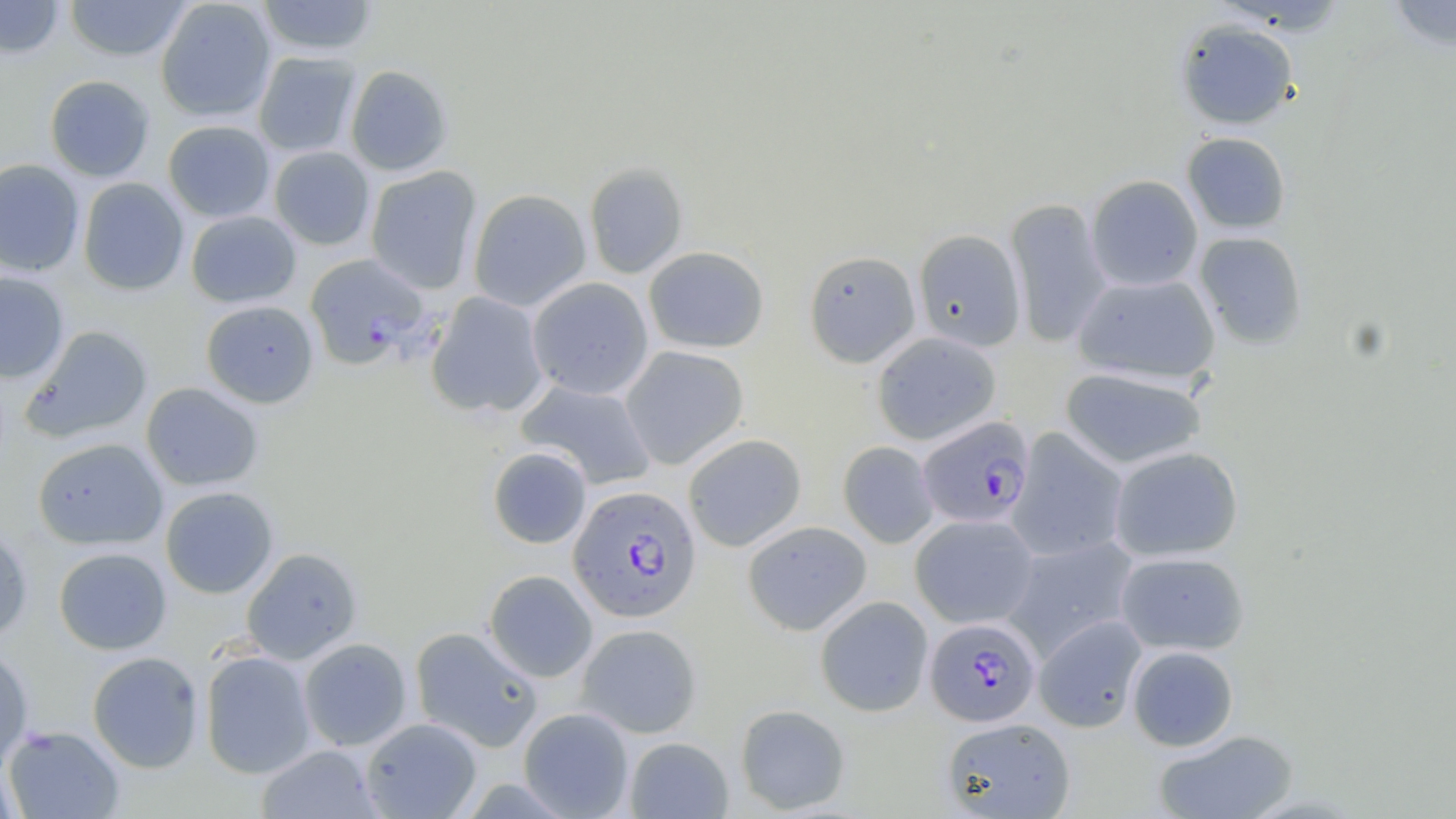
Approximate bounding boxes as named x1/y1/x2/y2 corners in pixels. Uninfected red blood cell locations: (x1=0, y1=0, x2=66, y2=59), (x1=63, y1=0, x2=193, y2=61), (x1=155, y1=0, x2=276, y2=122), (x1=255, y1=0, x2=380, y2=57), (x1=1383, y1=1, x2=1456, y2=52), (x1=1176, y1=19, x2=1299, y2=130), (x1=253, y1=52, x2=361, y2=158), (x1=345, y1=64, x2=453, y2=176), (x1=44, y1=75, x2=156, y2=182), (x1=163, y1=120, x2=275, y2=223), (x1=1181, y1=132, x2=1292, y2=234), (x1=269, y1=146, x2=375, y2=250), (x1=0, y1=158, x2=85, y2=277), (x1=584, y1=163, x2=688, y2=278), (x1=365, y1=166, x2=482, y2=294), (x1=1086, y1=174, x2=1203, y2=292), (x1=77, y1=177, x2=189, y2=295), (x1=468, y1=188, x2=592, y2=312), (x1=1004, y1=197, x2=1112, y2=349), (x1=185, y1=210, x2=301, y2=308), (x1=913, y1=228, x2=1026, y2=352), (x1=1193, y1=231, x2=1308, y2=349), (x1=643, y1=246, x2=769, y2=353), (x1=803, y1=249, x2=921, y2=368), (x1=0, y1=272, x2=69, y2=383), (x1=1072, y1=272, x2=1221, y2=386), (x1=527, y1=277, x2=653, y2=400), (x1=426, y1=292, x2=550, y2=419), (x1=200, y1=299, x2=319, y2=408), (x1=22, y1=325, x2=153, y2=443), (x1=872, y1=331, x2=1002, y2=445), (x1=621, y1=346, x2=749, y2=469), (x1=1059, y1=365, x2=1208, y2=469), (x1=515, y1=379, x2=657, y2=490), (x1=140, y1=382, x2=264, y2=491), (x1=1007, y1=428, x2=1129, y2=562), (x1=682, y1=433, x2=807, y2=551), (x1=33, y1=437, x2=168, y2=550), (x1=838, y1=441, x2=940, y2=548), (x1=487, y1=446, x2=592, y2=548), (x1=1108, y1=446, x2=1244, y2=562), (x1=160, y1=486, x2=279, y2=599), (x1=910, y1=514, x2=1040, y2=628), (x1=742, y1=520, x2=872, y2=635), (x1=0, y1=524, x2=33, y2=643), (x1=1002, y1=536, x2=1141, y2=659), (x1=53, y1=547, x2=172, y2=655), (x1=241, y1=547, x2=362, y2=665), (x1=1115, y1=551, x2=1250, y2=656), (x1=483, y1=569, x2=598, y2=682), (x1=814, y1=595, x2=934, y2=717), (x1=1034, y1=615, x2=1148, y2=733), (x1=576, y1=623, x2=702, y2=738), (x1=410, y1=626, x2=543, y2=751), (x1=298, y1=638, x2=412, y2=751), (x1=0, y1=645, x2=34, y2=774), (x1=1126, y1=645, x2=1239, y2=751), (x1=199, y1=650, x2=317, y2=779), (x1=87, y1=651, x2=205, y2=773), (x1=735, y1=703, x2=851, y2=814), (x1=518, y1=707, x2=634, y2=818), (x1=361, y1=717, x2=482, y2=818), (x1=941, y1=717, x2=1076, y2=818), (x1=3, y1=725, x2=125, y2=818), (x1=1152, y1=728, x2=1300, y2=818), (x1=624, y1=737, x2=733, y2=818), (x1=256, y1=744, x2=384, y2=818), (x1=0, y1=760, x2=20, y2=819). Plasmodium falciparum-infected red blood cell locations: (x1=304, y1=253, x2=429, y2=369), (x1=917, y1=416, x2=1035, y2=528), (x1=568, y1=485, x2=701, y2=623), (x1=925, y1=618, x2=1041, y2=727). Slide-level diagnosis: Plasmodium falciparum. May-Grünwald-Giemsa-stained preparation. Optical microscopy. One field of a larger specimen. 1000x magnification. Thin blood film. Image is 1456×819 pixels.